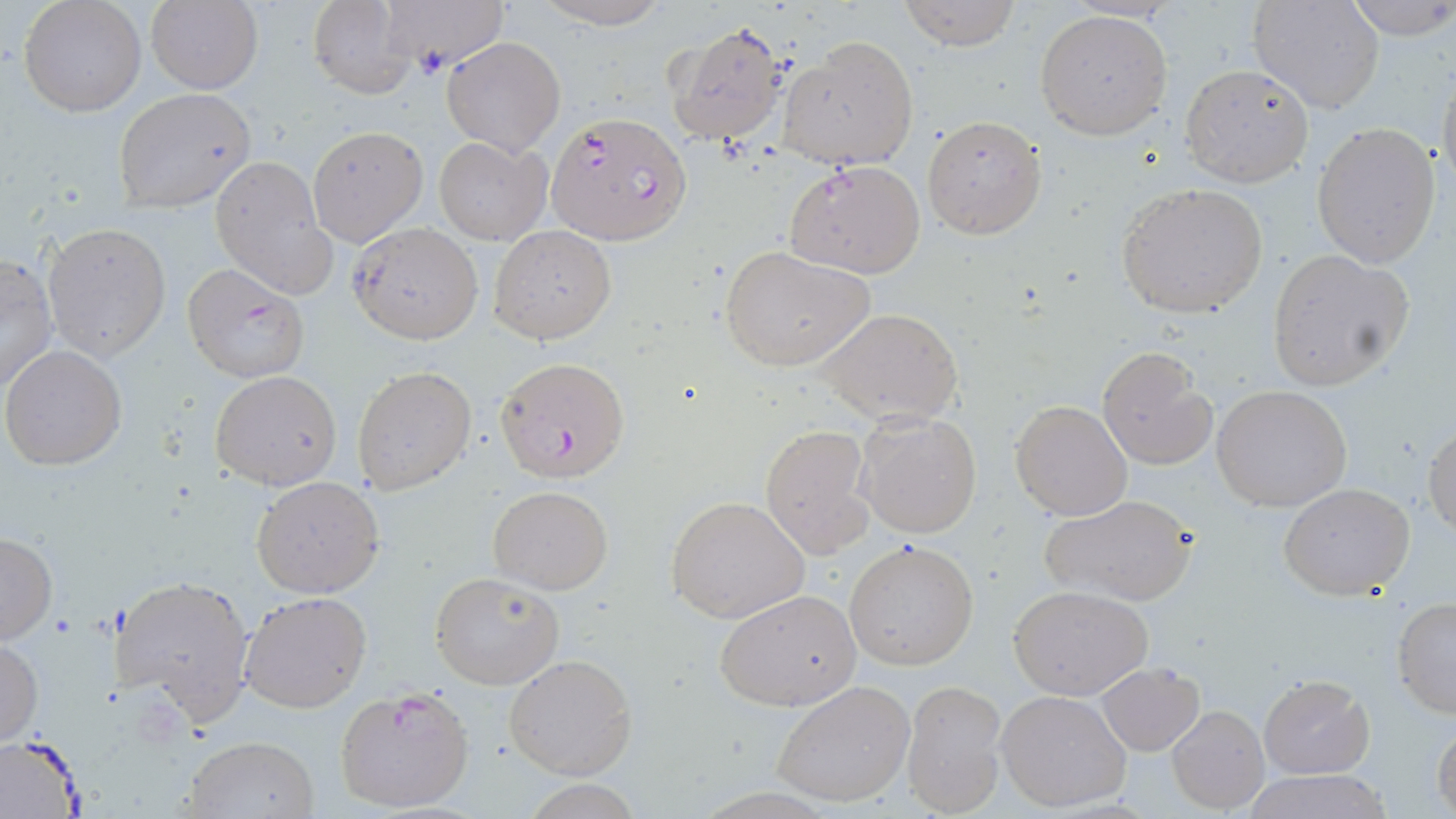
slide_level_diagnosis: Plasmodium falciparum
preparation: thin blood film
uninfected_red_blood_cell_locations_subset: 'approximate bounding boxes as (x1, y1, x2, y2) in pixels: (18, 0, 147, 117), (305, 0, 417, 98), (382, 0, 510, 69), (534, 0, 672, 28), (899, 0, 1019, 50), (1248, 0, 1384, 115), (1345, 0, 1456, 40), (146, 1, 262, 92), (1034, 9, 1173, 141), (662, 20, 791, 148), (441, 36, 566, 155), (776, 36, 919, 170), (1179, 63, 1314, 188), (1436, 68, 1456, 205), (113, 87, 256, 212), (922, 115, 1046, 239), (1311, 122, 1441, 269), (308, 125, 428, 246), (434, 137, 551, 244), (211, 157, 335, 298), (1115, 181, 1270, 321), (43, 221, 171, 361), (350, 222, 483, 343), (489, 225, 616, 345), (718, 243, 875, 373), (1264, 249, 1415, 392), (1, 254, 58, 396), (818, 308, 964, 425), (2, 344, 127, 470), (1096, 347, 1215, 470), (352, 365, 477, 495), (210, 370, 342, 490), (1212, 384, 1352, 512), (1009, 399, 1133, 520), (855, 408, 982, 539), (1424, 419, 1456, 536), (759, 424, 875, 558), (250, 475, 384, 598), (1279, 482, 1416, 600), (489, 485, 612, 594), (1040, 493, 1198, 607), (666, 495, 811, 624), (0, 530, 57, 645), (845, 539, 979, 670), (429, 570, 565, 690), (111, 573, 255, 722), (1009, 584, 1152, 700), (716, 589, 862, 711), (240, 591, 370, 713), (1391, 599, 1456, 718), (0, 634, 43, 750), (503, 653, 637, 779), (1097, 661, 1205, 754), (1259, 674, 1374, 778), (772, 679, 917, 807), (901, 680, 1007, 818), (997, 690, 1132, 812), (1166, 705, 1269, 814), (1432, 723, 1456, 818), (1, 734, 86, 816), (180, 734, 319, 818), (1246, 769, 1393, 819)'
field_of_view: single
image_size: 1456×819 pixels
magnification: 1000x
plasmodium_falciparum_infected_red_blood_cell_locations_subset: 'approximate bounding boxes as (x1, y1, x2, y2) in pixels: (548, 111, 693, 246), (785, 160, 926, 279), (181, 263, 310, 383), (335, 684, 475, 815)'
modality: optical microscopy
stain: May-Grünwald-Giemsa